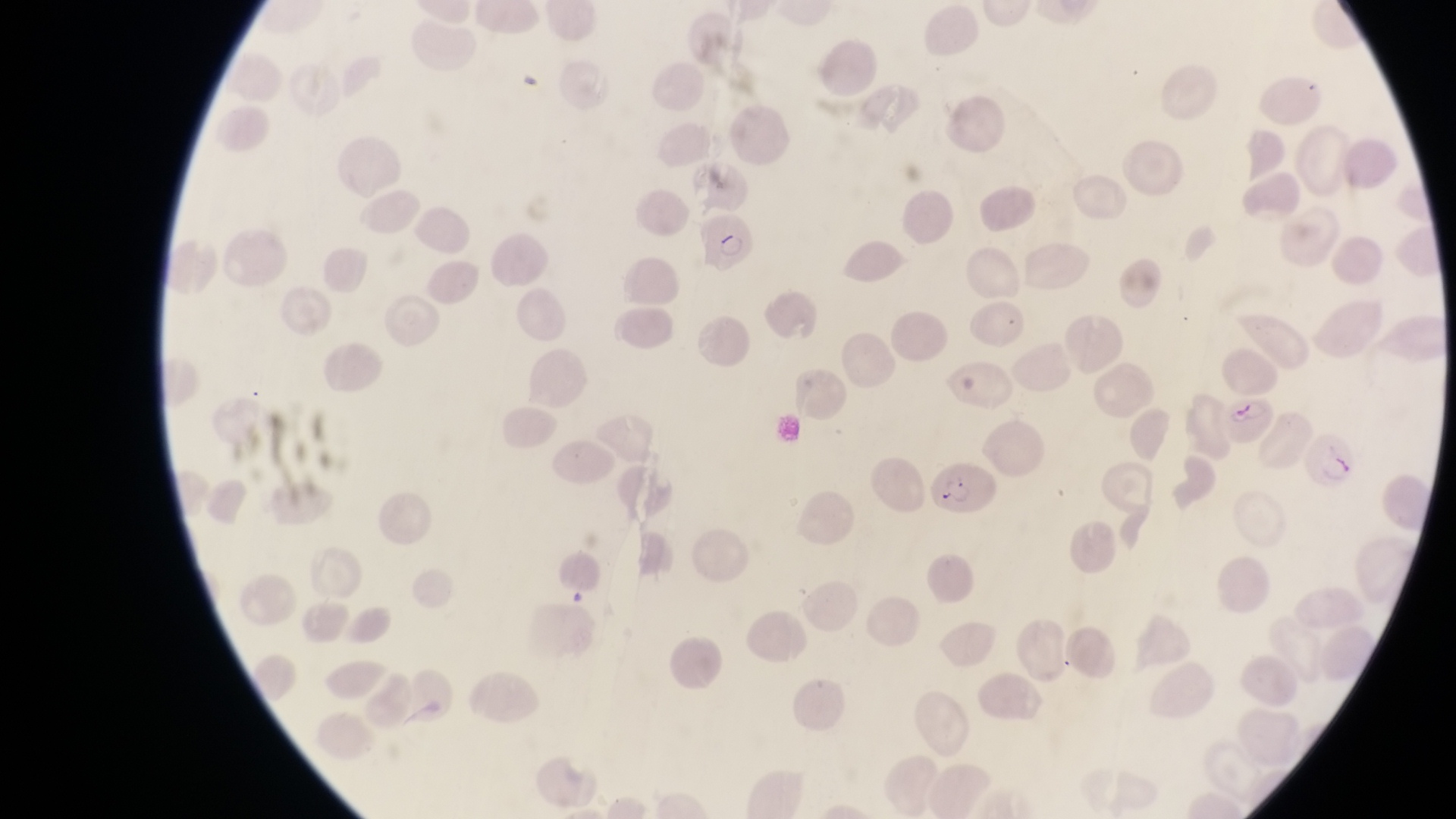 Approximate bounding boxes as {left, top, right, bottom} in pixels. Parasitised red blood cell locations: {697, 212, 755, 270}, {1219, 389, 1277, 444}, {1304, 433, 1360, 489}, {930, 460, 999, 516}. At a magnification of 1000x. Image is 1456×819 pixels. Sample from Uganda. Single field of view. Photographed through the eyepiece of an Olympus CX-23 microscope with a smartphone camera. Thin blood smear.